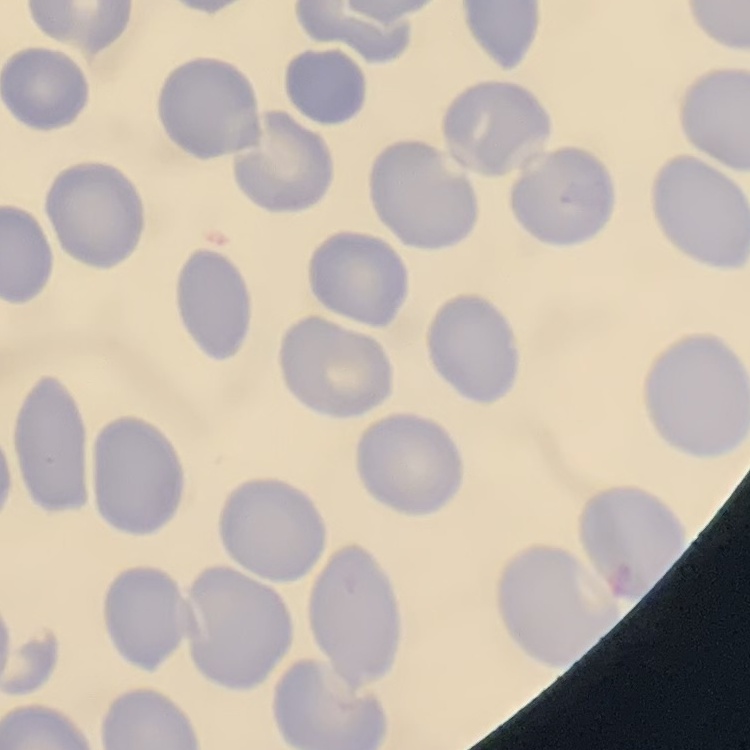
The red blood cells show no rouleaux formation. Square crop of a larger photomicrograph. Thin peripheral smear. Field's or Giemsa stain.